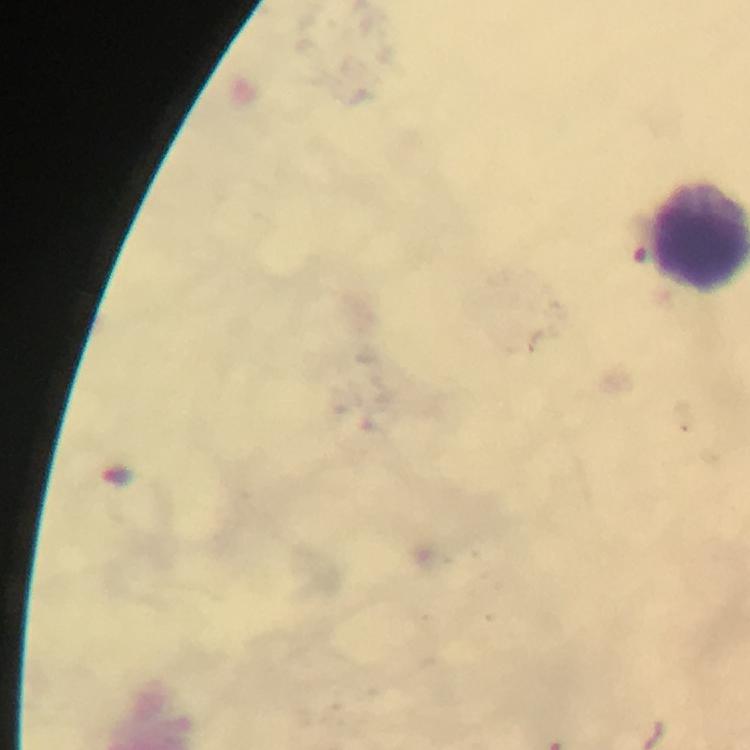

Approximate object centers, in pixels from the top-left corner.
Summary:
  - Leukocyte locations: (x=701, y=234)
  - Preparation: thick blood smear
  - Capture: smartphone camera through the microscope
  - Magnification: 100x
  - Context: from a malaria diagnostic workup
  - Immersion oil: applied
  - Malaria parasites: none detected
  - Stain: Giemsa
  - Image size: 750×750 pixels
  - Cropped from: one field of view